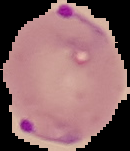 Image is 130×151 pixels. Segmented cell region on a black background. From a thin blood smear. Malaria status: parasitized.